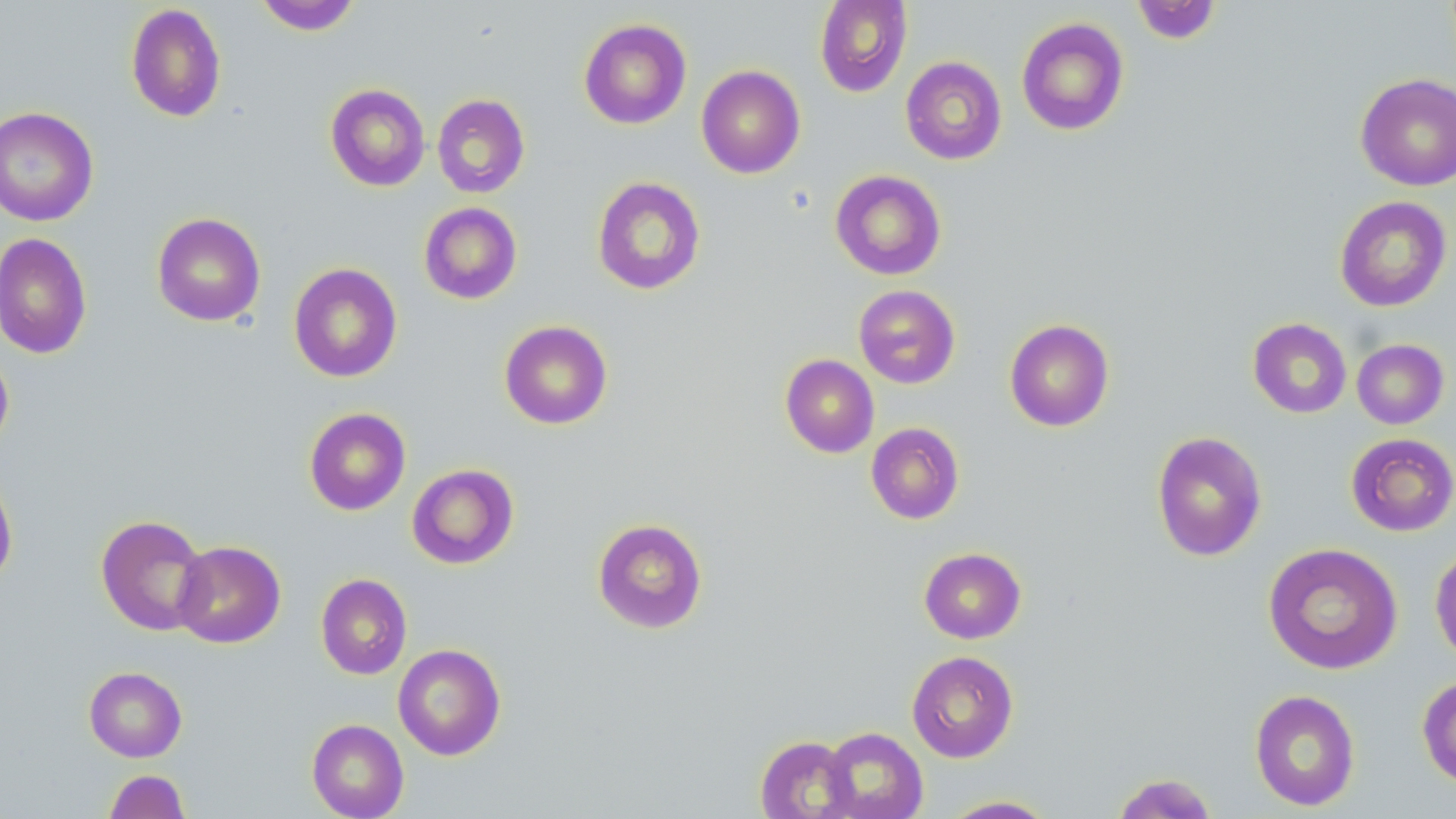

slide-level diagnosis = negative for blood parasites
magnification = 1000x
preparation = thin blood smear
stain = May-Grünwald-Giemsa
modality = optical microscopy
image size = 1456×819 pixels
field of view = single
uninfected red blood cell locations = approximate bounding boxes as (x1, y1, x2, y2) in pixels: (253, 0, 363, 35), (814, 0, 912, 97), (1131, 0, 1222, 44), (125, 3, 227, 122), (1016, 17, 1129, 136), (578, 18, 692, 129), (900, 56, 1007, 165), (696, 65, 805, 179), (1355, 73, 1456, 191), (325, 83, 430, 192), (432, 93, 530, 198), (0, 106, 99, 227), (830, 169, 946, 280), (591, 175, 706, 295), (1334, 195, 1452, 312), (419, 202, 522, 304), (151, 212, 266, 327), (0, 232, 92, 359), (288, 262, 403, 382), (853, 284, 961, 389), (1247, 317, 1352, 418), (1004, 319, 1114, 432), (499, 320, 613, 429), (1352, 339, 1449, 429), (0, 348, 14, 454), (780, 354, 879, 458), (304, 407, 411, 515), (865, 422, 965, 524), (1151, 430, 1268, 562), (1346, 433, 1456, 536), (407, 463, 519, 569), (0, 471, 18, 587), (96, 514, 209, 636), (592, 518, 708, 634), (172, 540, 285, 648), (1262, 542, 1403, 675), (1430, 544, 1456, 667), (919, 547, 1027, 644), (316, 573, 412, 680), (393, 643, 506, 761), (907, 650, 1019, 763), (84, 666, 187, 762), (1416, 674, 1456, 787), (1249, 688, 1361, 811), (306, 718, 409, 819), (820, 726, 928, 819), (754, 735, 859, 819), (103, 770, 190, 818), (1111, 772, 1218, 818), (940, 795, 1059, 818)